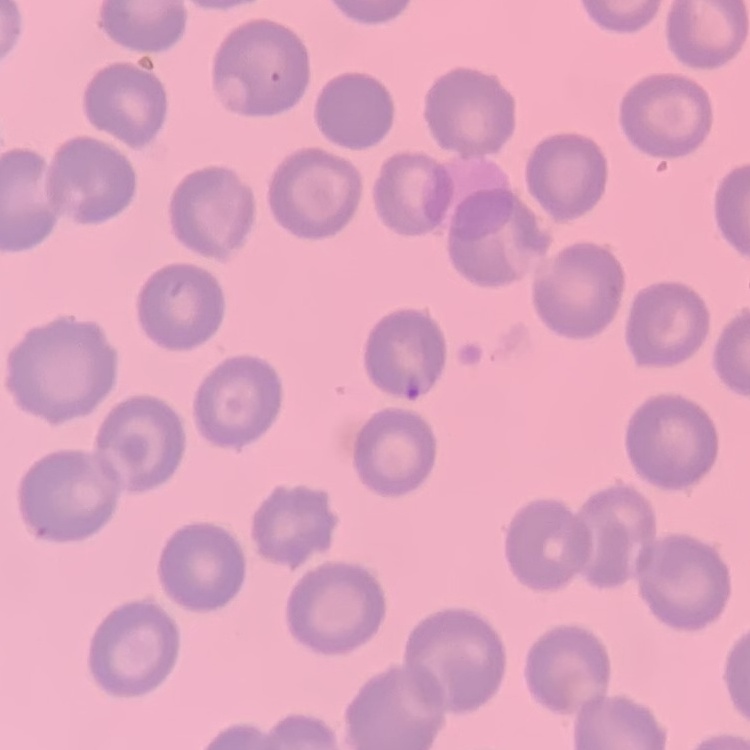
The red blood cells show no rouleaux formation. Thin blood film. Field's or Giemsa stain. Square crop of a larger photomicrograph.